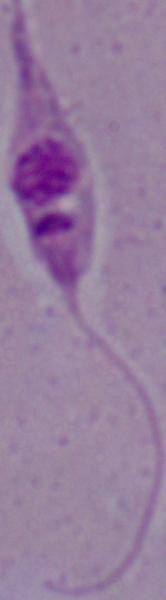
{
  "identification": "Leishmania",
  "modality": "micrograph",
  "magnification": "1000x"
}